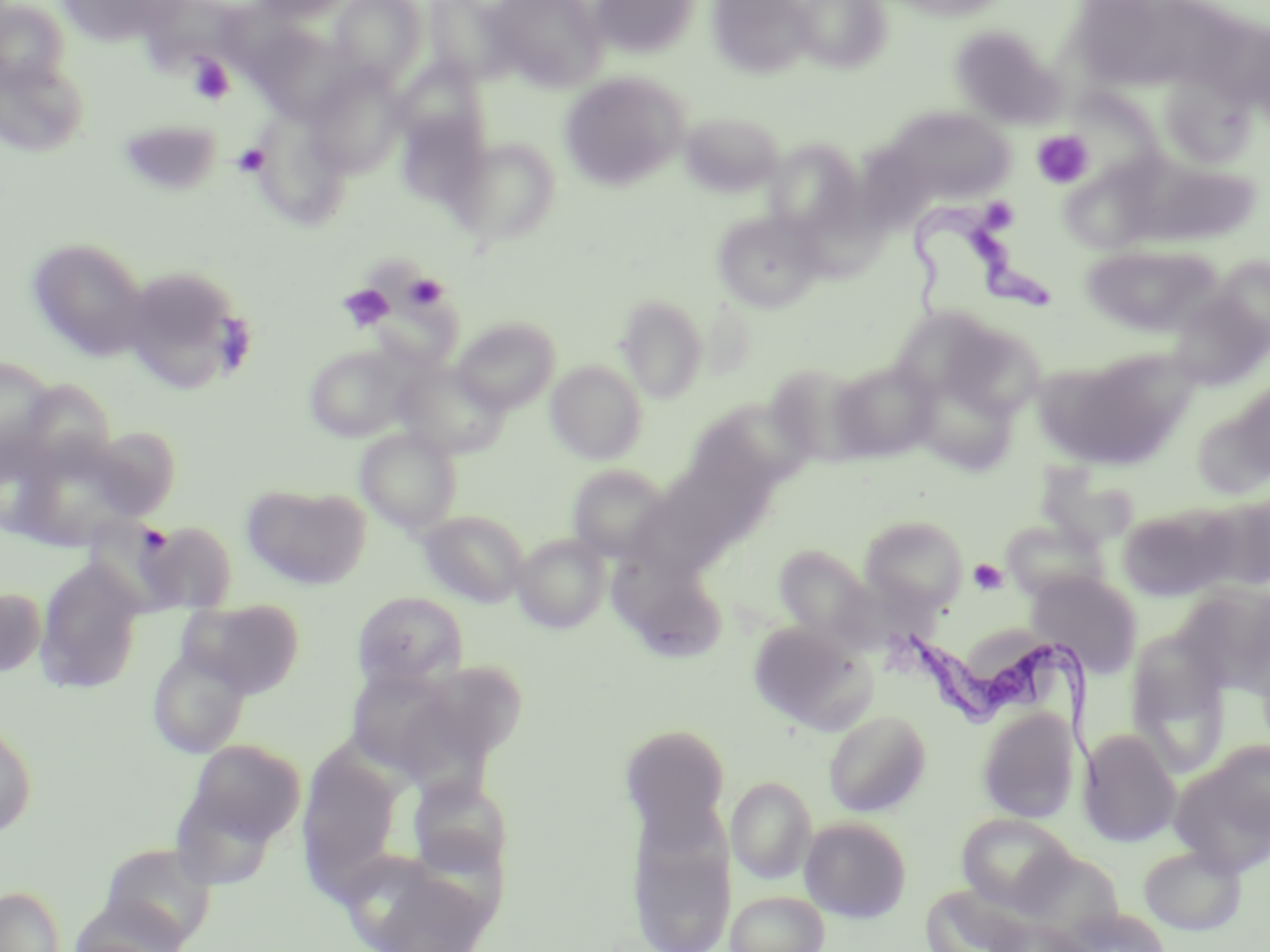

{
  "trypanosoma_brucei_locations": "approximate bounding boxes as named x1/y1/x2/y2 corners in pixels: (x1=902, y1=189, x2=1061, y2=329), (x1=890, y1=620, x2=1113, y2=789)",
  "slide_level_diagnosis": "Trypanosoma brucei",
  "stain": "May-Grünwald-Giemsa",
  "preparation": "thin blood smear",
  "magnification": "1000x",
  "field_of_view": "single",
  "image_size": "1270×952 pixels",
  "platelet_locations": "approximate bounding boxes as named x1/y1/x2/y2 corners in pixels: (x1=189, y1=55, x2=234, y2=104), (x1=1032, y1=130, x2=1095, y2=189), (x1=233, y1=142, x2=269, y2=176), (x1=982, y1=201, x2=1019, y2=236), (x1=404, y1=273, x2=449, y2=310), (x1=339, y1=284, x2=394, y2=332), (x1=969, y1=558, x2=1008, y2=595)",
  "uninfected_red_blood_cell_locations": "approximate bounding boxes as named x1/y1/x2/y2 corners in pixels: (x1=58, y1=0, x2=183, y2=46), (x1=251, y1=0, x2=353, y2=23), (x1=330, y1=0, x2=427, y2=87), (x1=426, y1=0, x2=520, y2=86), (x1=487, y1=0, x2=608, y2=91), (x1=588, y1=0, x2=701, y2=59), (x1=707, y1=0, x2=815, y2=78), (x1=789, y1=0, x2=892, y2=72), (x1=880, y1=0, x2=1014, y2=21), (x1=0, y1=2, x2=69, y2=92), (x1=248, y1=23, x2=356, y2=124), (x1=949, y1=25, x2=1067, y2=129), (x1=0, y1=57, x2=90, y2=158), (x1=392, y1=59, x2=490, y2=159), (x1=305, y1=65, x2=408, y2=178), (x1=559, y1=72, x2=689, y2=192), (x1=1160, y1=72, x2=1257, y2=171), (x1=887, y1=106, x2=1015, y2=203), (x1=396, y1=109, x2=489, y2=209), (x1=681, y1=112, x2=783, y2=197), (x1=118, y1=120, x2=222, y2=196), (x1=254, y1=121, x2=349, y2=226), (x1=451, y1=137, x2=561, y2=246), (x1=764, y1=140, x2=863, y2=236), (x1=1135, y1=159, x2=1262, y2=247), (x1=1067, y1=160, x2=1168, y2=252), (x1=712, y1=210, x2=826, y2=313), (x1=27, y1=238, x2=149, y2=361), (x1=1081, y1=243, x2=1223, y2=338), (x1=1213, y1=256, x2=1270, y2=351), (x1=136, y1=276, x2=243, y2=388), (x1=1165, y1=289, x2=1270, y2=391), (x1=616, y1=295, x2=709, y2=403), (x1=887, y1=305, x2=1009, y2=410), (x1=452, y1=317, x2=560, y2=414), (x1=304, y1=345, x2=412, y2=442), (x1=1044, y1=352, x2=1185, y2=470), (x1=0, y1=355, x2=58, y2=471), (x1=546, y1=360, x2=648, y2=465), (x1=828, y1=360, x2=938, y2=462), (x1=393, y1=361, x2=509, y2=459), (x1=769, y1=365, x2=861, y2=471), (x1=913, y1=368, x2=1020, y2=475), (x1=690, y1=402, x2=815, y2=487), (x1=1194, y1=405, x2=1270, y2=487), (x1=84, y1=425, x2=182, y2=522), (x1=356, y1=428, x2=462, y2=533), (x1=567, y1=464, x2=673, y2=562), (x1=241, y1=482, x2=371, y2=590), (x1=1201, y1=488, x2=1270, y2=592), (x1=1117, y1=505, x2=1232, y2=600), (x1=417, y1=510, x2=528, y2=607), (x1=860, y1=515, x2=967, y2=613), (x1=1001, y1=518, x2=1110, y2=602), (x1=138, y1=519, x2=238, y2=613), (x1=513, y1=534, x2=610, y2=632), (x1=773, y1=545, x2=876, y2=644), (x1=608, y1=550, x2=729, y2=662), (x1=34, y1=557, x2=146, y2=694), (x1=1026, y1=569, x2=1144, y2=677), (x1=1176, y1=583, x2=1270, y2=700), (x1=0, y1=585, x2=47, y2=678), (x1=352, y1=591, x2=468, y2=689), (x1=178, y1=598, x2=305, y2=697), (x1=747, y1=620, x2=874, y2=733), (x1=1127, y1=633, x2=1231, y2=777), (x1=147, y1=646, x2=251, y2=758), (x1=437, y1=663, x2=527, y2=755), (x1=343, y1=665, x2=473, y2=778), (x1=977, y1=706, x2=1080, y2=823), (x1=824, y1=709, x2=931, y2=816), (x1=0, y1=716, x2=37, y2=841), (x1=619, y1=723, x2=732, y2=839), (x1=1078, y1=728, x2=1181, y2=847), (x1=182, y1=738, x2=306, y2=853), (x1=1170, y1=744, x2=1270, y2=875), (x1=405, y1=774, x2=514, y2=879), (x1=727, y1=776, x2=816, y2=884), (x1=625, y1=799, x2=736, y2=952), (x1=956, y1=814, x2=1075, y2=911), (x1=801, y1=817, x2=911, y2=923), (x1=99, y1=843, x2=219, y2=949), (x1=1138, y1=845, x2=1246, y2=935), (x1=340, y1=848, x2=496, y2=952), (x1=0, y1=885, x2=66, y2=952), (x1=924, y1=887, x2=1030, y2=950), (x1=727, y1=890, x2=828, y2=952), (x1=68, y1=904, x2=194, y2=952), (x1=1062, y1=906, x2=1172, y2=952), (x1=986, y1=916, x2=1090, y2=952)",
  "modality": "light microscopy"
}